Assess this cell for malaria.
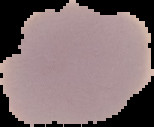
It is uninfected.

{
  "image_type": "cell region segmented out of the field of view; surrounding area masked to black",
  "image_size": "154×127 pixels",
  "preparation": "thin blood film"
}